Locate every blood parasite and identify its species.
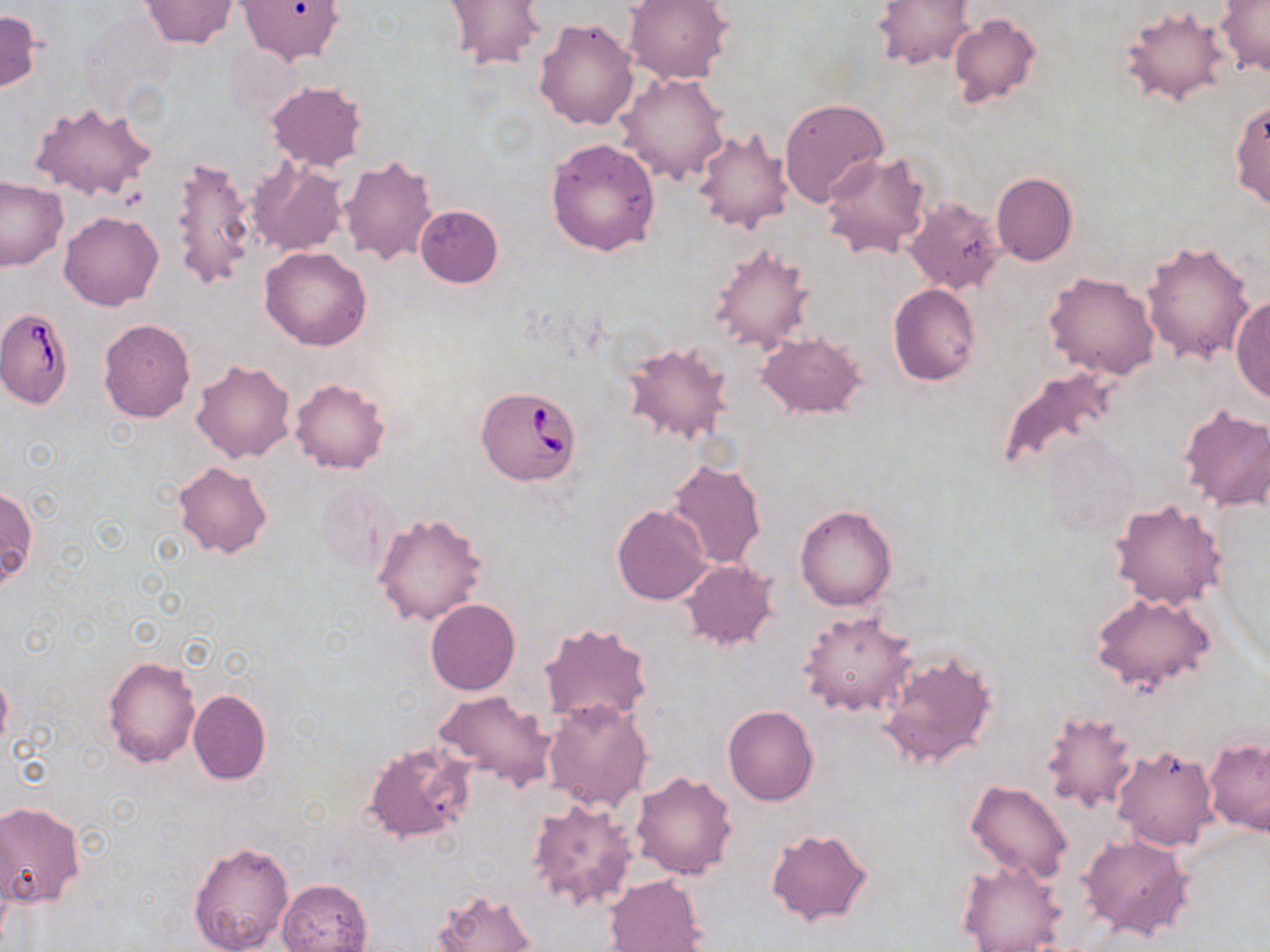
Approximate bounding boxes as [x1, y1, x2, y2] in pixels.
Babesia divergens-infected red blood cells: [0, 306, 74, 411], [475, 386, 582, 486].
No Plasmodium falciparum, Plasmodium ovale, Plasmodium malariae, Plasmodium vivax, or Trypanosoma brucei observed.

Summary:
  - Uninfected red blood cell locations: [139, 0, 239, 48], [237, 0, 344, 66], [440, 0, 547, 72], [625, 0, 732, 85], [873, 0, 973, 70], [1215, 0, 1269, 77], [1118, 6, 1232, 108], [0, 10, 42, 94], [947, 14, 1041, 106], [534, 17, 641, 130], [616, 71, 730, 185], [266, 81, 366, 169], [634, 91, 770, 213], [778, 98, 889, 208], [1230, 98, 1270, 214], [29, 100, 158, 203], [692, 127, 793, 234], [546, 137, 661, 257], [820, 151, 934, 260], [171, 154, 256, 292], [339, 154, 438, 267], [247, 157, 346, 257], [992, 173, 1077, 266], [0, 176, 68, 271], [904, 197, 1004, 295], [414, 206, 504, 288], [60, 210, 165, 310], [1140, 241, 1256, 368], [707, 242, 815, 354], [259, 246, 372, 350], [1043, 270, 1161, 380], [888, 284, 981, 386], [1230, 293, 1270, 404], [98, 318, 196, 423], [757, 331, 866, 418], [622, 339, 733, 444], [190, 359, 295, 463], [992, 366, 1119, 481], [290, 378, 390, 473], [1179, 403, 1270, 512], [664, 459, 768, 570], [172, 460, 272, 558], [1, 486, 36, 589], [1108, 497, 1227, 610], [612, 504, 712, 605], [795, 504, 898, 611], [372, 512, 488, 626], [680, 561, 777, 652], [1089, 591, 1216, 694], [426, 598, 520, 695], [798, 609, 917, 718], [538, 621, 653, 727], [877, 650, 997, 770], [103, 655, 202, 766], [0, 670, 12, 754], [187, 689, 271, 785], [434, 690, 558, 791], [542, 698, 652, 811], [723, 705, 819, 805], [1040, 709, 1139, 813], [1204, 737, 1270, 835], [362, 741, 476, 845], [1112, 745, 1218, 850], [630, 771, 738, 879], [964, 778, 1073, 885], [526, 798, 640, 913], [0, 801, 85, 906], [766, 828, 873, 926], [1079, 833, 1193, 939], [187, 840, 294, 952], [955, 859, 1066, 951], [602, 875, 707, 952], [276, 879, 373, 952], [429, 888, 537, 952]
  - Slide-level diagnosis: Babesia divergens
  - Magnification: 1000x
  - Image size: 1270×952 pixels
  - Modality: optical microscopy
  - Stain: May-Grünwald-Giemsa
  - Field of view: single
  - Preparation: thin blood film